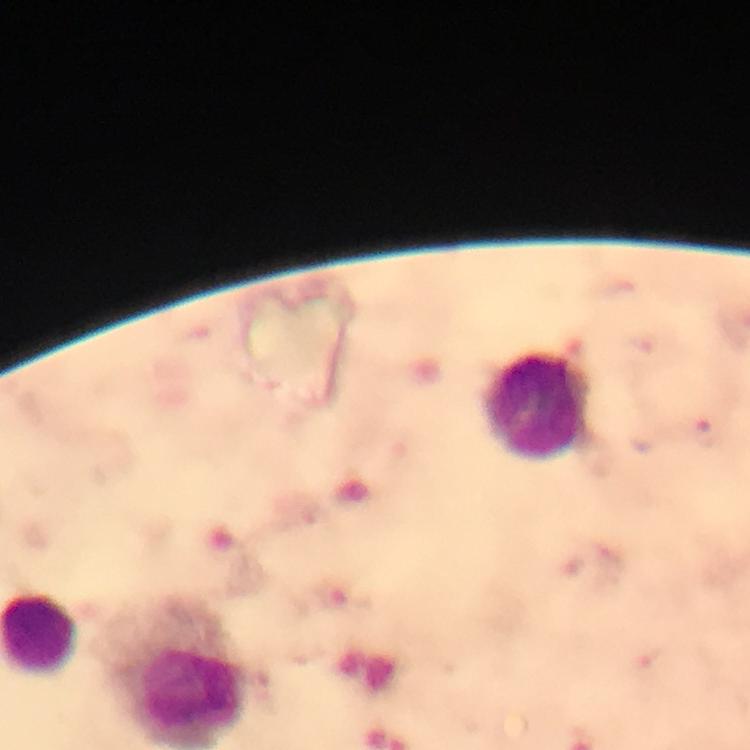

Approximate centers as {x, y} in pixels.
Summary:
  - Leukocyte locations: {536, 407}
  - Cropped from: one field of view
  - Magnification: 100x
  - Stain: Giemsa
  - Context: from a malaria diagnostic workup
  - Image size: 750×750 pixels
  - Malaria parasites: none detected
  - Preparation: thick smear
  - Immersion oil: used
  - Capture: smartphone mounted on the microscope